Name the blood parasite species.
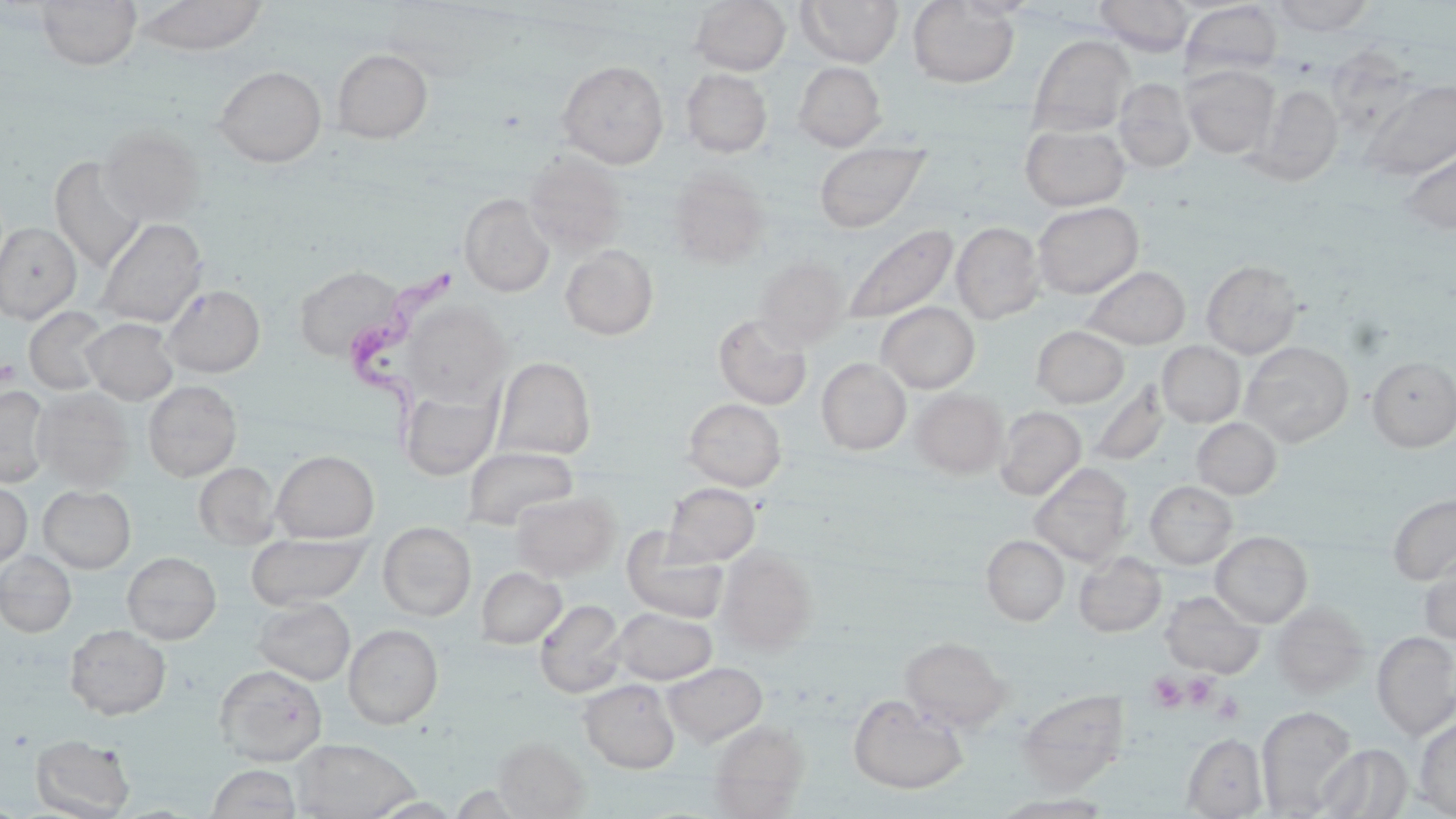
Trypanosoma brucei.

Approximate bounding boxes as (x1, y1, x2, y2) in pixels. Uninfected red blood cell locations: (36, 0, 142, 70), (138, 0, 267, 56), (690, 0, 791, 75), (796, 0, 903, 67), (953, 0, 1040, 19), (1095, 0, 1193, 56), (1270, 0, 1376, 35), (907, 1, 1020, 89), (1180, 2, 1282, 81), (1029, 34, 1135, 135), (331, 49, 433, 143), (557, 60, 669, 168), (793, 62, 887, 151), (1182, 64, 1278, 159), (213, 65, 327, 167), (681, 68, 772, 158), (1114, 78, 1196, 173), (1362, 78, 1456, 181), (1253, 83, 1345, 185), (1020, 123, 1129, 211), (99, 125, 207, 226), (813, 141, 930, 233), (1398, 143, 1456, 235), (523, 151, 628, 253), (49, 156, 145, 273), (668, 169, 769, 268), (459, 194, 555, 297), (1033, 201, 1143, 299), (95, 218, 207, 328), (0, 221, 81, 323), (952, 222, 1045, 324), (842, 223, 959, 326), (560, 245, 659, 340), (754, 256, 849, 350), (1201, 259, 1303, 358), (295, 263, 403, 361), (1083, 265, 1190, 349), (162, 284, 266, 377), (403, 301, 512, 406), (877, 302, 980, 393), (24, 306, 114, 394), (712, 312, 813, 410), (82, 318, 179, 404), (1031, 326, 1129, 408), (1241, 341, 1354, 447), (1157, 342, 1245, 427), (493, 356, 596, 459), (1367, 356, 1456, 451), (816, 358, 911, 455), (1085, 379, 1168, 468), (143, 380, 242, 481), (0, 386, 51, 487), (400, 387, 499, 479), (33, 388, 134, 491), (910, 388, 1008, 478), (683, 398, 787, 491), (994, 406, 1086, 500), (1192, 418, 1281, 499), (462, 446, 579, 531), (271, 450, 379, 542), (194, 462, 281, 550), (1030, 462, 1133, 566), (1145, 480, 1237, 568), (0, 481, 32, 569), (663, 482, 760, 566), (38, 485, 136, 573), (511, 491, 620, 581), (1388, 493, 1456, 585), (378, 522, 476, 621), (621, 528, 728, 623), (1210, 531, 1312, 627), (245, 532, 369, 610), (981, 535, 1069, 626), (716, 546, 817, 653), (0, 551, 76, 638), (121, 551, 221, 644), (1074, 552, 1166, 637), (1419, 557, 1456, 645), (477, 566, 566, 648), (1160, 591, 1263, 677), (1162, 596, 1371, 680), (253, 597, 355, 685), (535, 600, 626, 698), (1271, 601, 1370, 697), (611, 608, 717, 684), (64, 624, 171, 720), (344, 625, 443, 729), (1372, 632, 1456, 740), (900, 637, 1012, 732), (663, 662, 767, 746), (214, 664, 327, 766), (579, 679, 680, 773), (1018, 689, 1129, 791), (848, 694, 968, 794), (1257, 706, 1357, 816), (1415, 716, 1456, 818), (709, 720, 809, 816), (1182, 733, 1268, 817), (29, 734, 136, 818), (493, 736, 589, 818), (291, 738, 422, 819), (1314, 743, 1413, 818), (206, 764, 302, 819), (994, 794, 1113, 817). Trypanosoma brucei locations: (343, 267, 460, 446). Platelet locations: (1, 359, 19, 386), (1184, 673, 1217, 707), (1147, 674, 1188, 711), (1212, 693, 1245, 725). May-Grünwald-Giemsa-stained preparation. Image is 1456×819 pixels. Optical microscopy. One field of a larger specimen. Thin blood film. Captured at 1000x magnification.